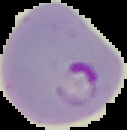
Segmented cell region on a black background. Result: malaria parasites identified. Image is 127×130 pixels. From a thin blood film.